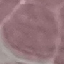
Summary:
  - Malaria status: uninfected
  - Image type: cell patch, automatically extracted from a larger field of view and resized to 64 × 64 pixels
  - Capture: smartphone through the microscope eyepiece
  - Stain: Giemsa
  - Preparation: thin blood film